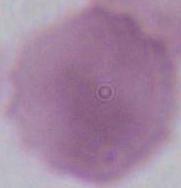

identification = erythrocyte
modality = photomicrograph
magnification = 1000x